Assess this cell for malaria.
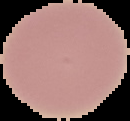

Uninfected.

Summary:
  - Image size: 130×121 pixels
  - Image type: segmented cell region with the area outside set to black
  - Preparation: thin blood smear